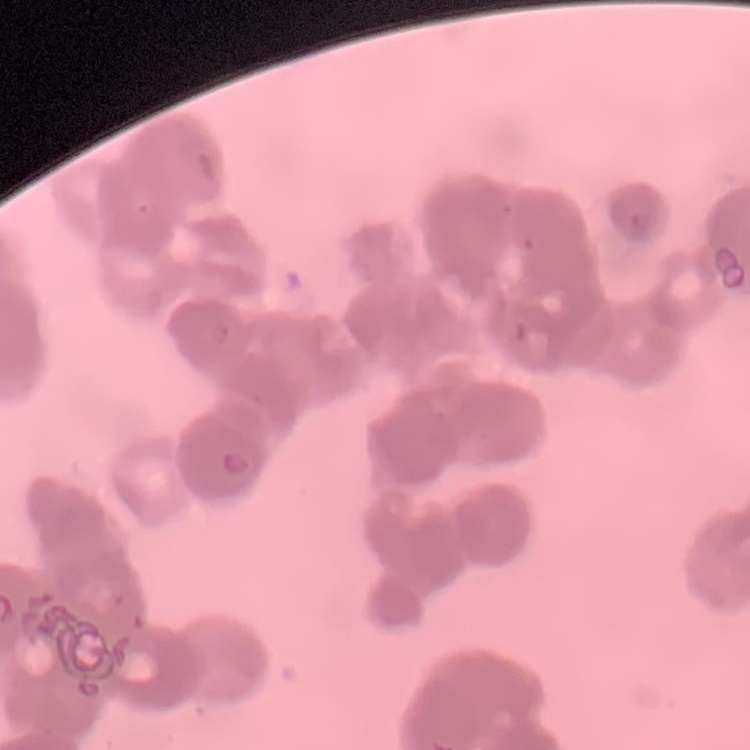

The red blood cells exhibit rouleaux formation. Thin blood smear. One tile cut from a larger photomicrograph. Stained with either Field's or Giemsa.